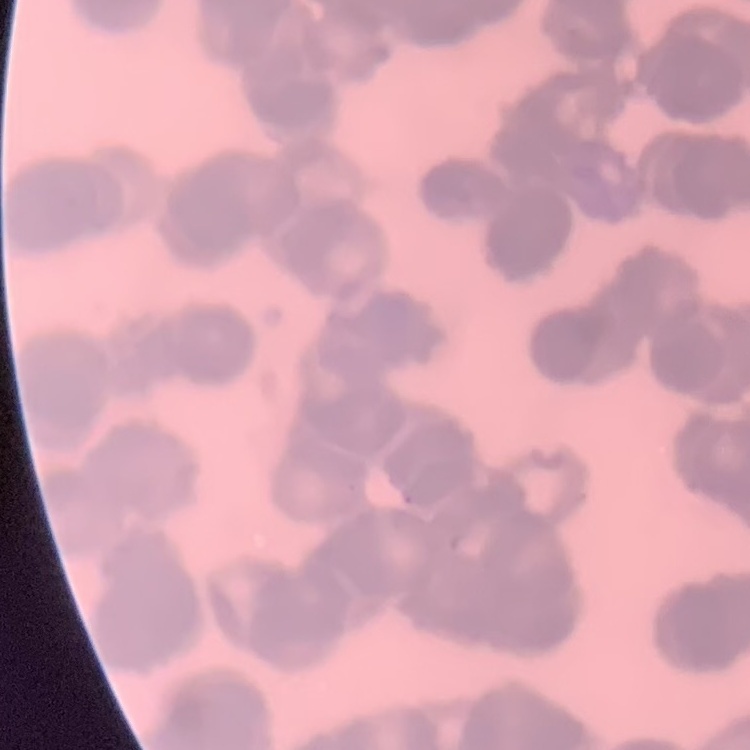
red blood cell morphology = rouleaux formation
stain = Field's or Giemsa
image type = square crop of a larger photomicrograph
preparation = thin blood smear